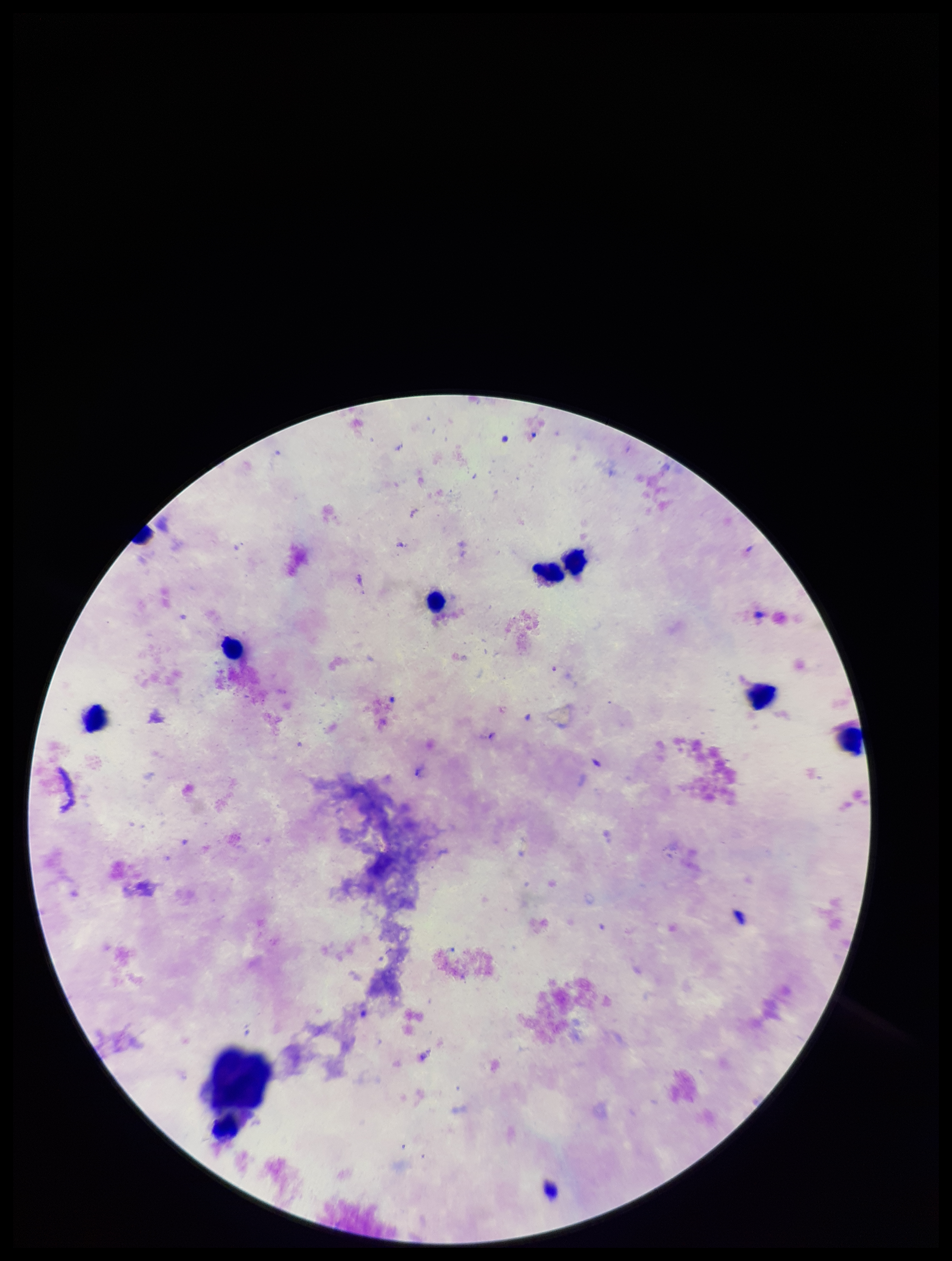 Patient malaria status: negative. Image is 952×1261 pixels. One field from this slide. Leukocyte count: 7. Photographed through the microscope eyepiece with a smartphone camera. Preparation: thick blood smear. Plasmodium parasites: none identified. Stained with Giemsa. Parasite count: 0.